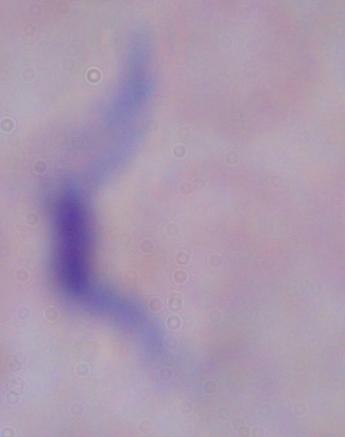

modality = micrograph
magnification = 1000x
identification = trypanosome